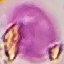
{
  "malaria_status": "uninfected",
  "capture": "smartphone camera at the microscope eyepiece",
  "stain": "Giemsa",
  "preparation": "thin smear",
  "image_type": "automatically extracted cell patch, resized to 64 × 64 pixels"
}